Mark where leukocytes are.
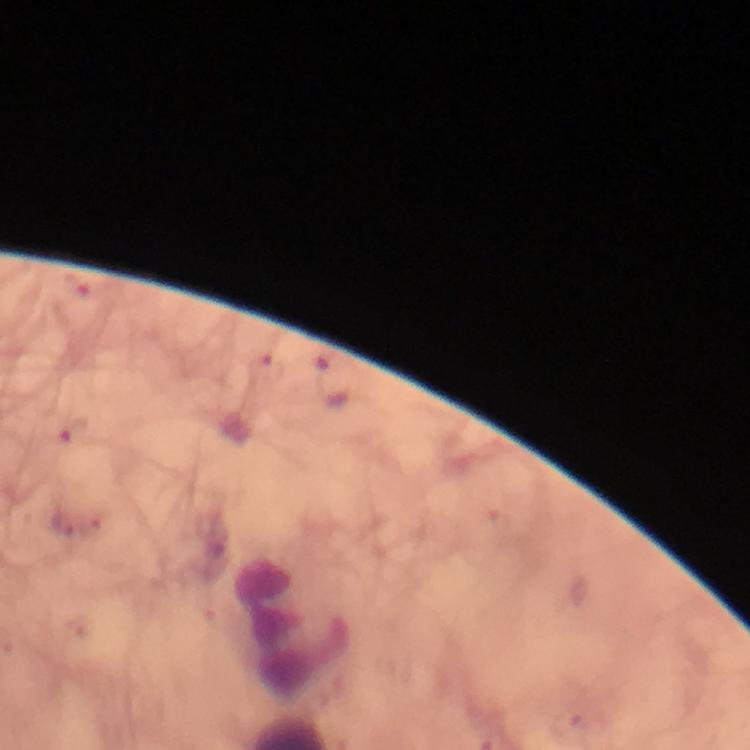

Approximate centers as {x, y} in pixels.
Leukocytes: {295, 627}.

{
  "magnification": "100x",
  "image_size": "750×750 pixels",
  "capture": "smartphone photograph through a microscope",
  "malaria_parasite_locations": "approximate centers as {x, y} in pixels: {65, 524}",
  "immersion_oil": "applied",
  "stain": "Giemsa",
  "context": "from a diagnostic examination for malaria",
  "preparation": "thick blood film",
  "cropped_from": "a single field of view"
}